Describe the morphology of the red blood cells.
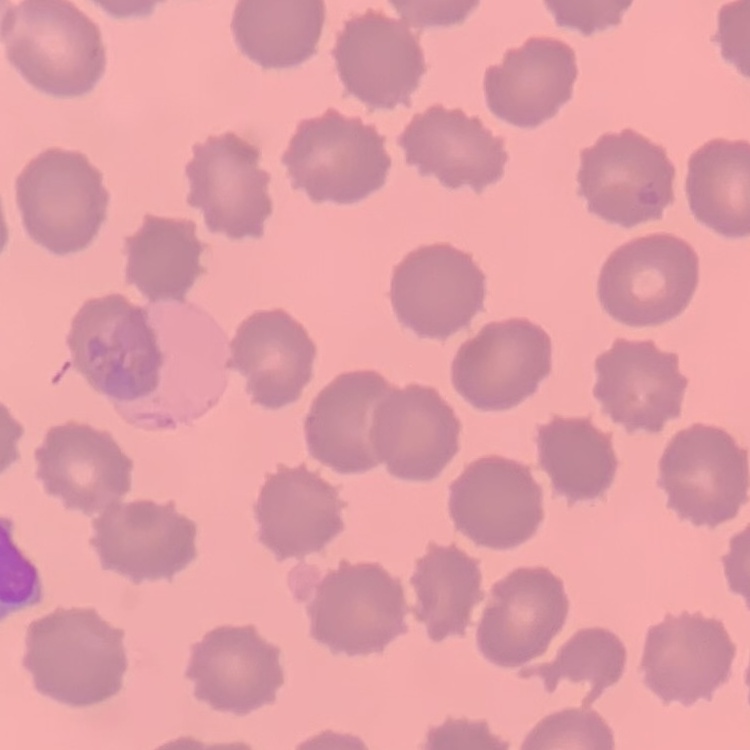

They show no rouleaux formation.

image type = one tile cut from a larger photomicrograph
preparation = thin blood smear
stain = Field's or Giemsa